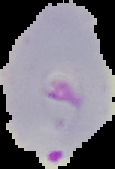

Summary:
  - Image type: segmented cell region on a black background
  - Preparation: thin blood film
  - Image size: 115×169 pixels
  - Result: malaria parasites identified